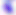
modality = photomicrograph
identification = Toxoplasma gondii
magnification = 400x